Give the extent of all Plasmodium falciparum-infected red blood cells.
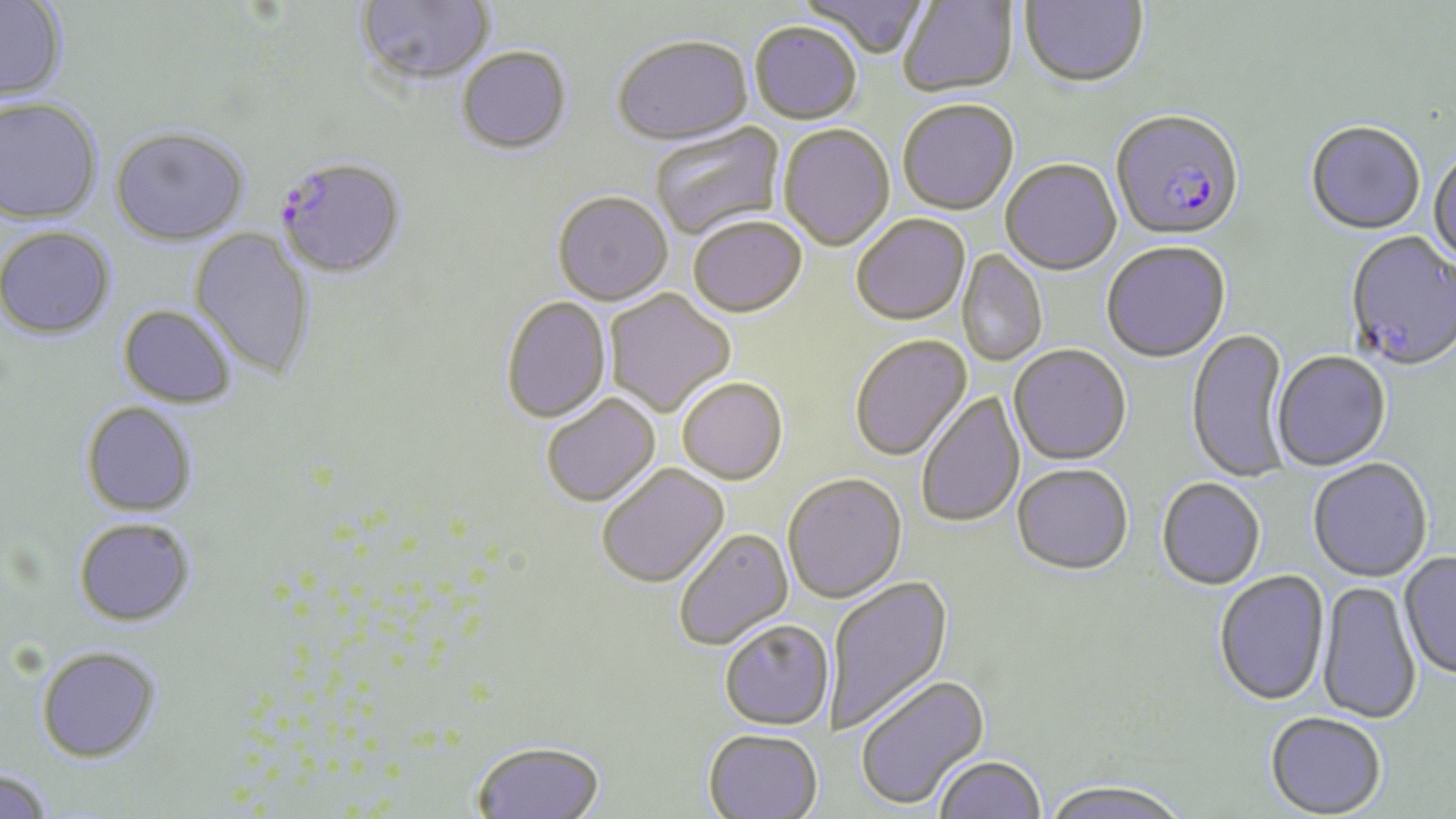
Approximate bounding boxes as [x1, y1, x2, y2] in pixels.
Plasmodium falciparum-infected red blood cells: [1110, 113, 1244, 244], [276, 157, 407, 279].

Summary:
  - Uninfected red blood cell locations: [355, 0, 494, 86], [797, 0, 930, 61], [898, 0, 1018, 98], [1020, 0, 1149, 89], [0, 1, 68, 101], [749, 24, 862, 125], [612, 37, 752, 148], [456, 47, 572, 155], [0, 96, 103, 224], [898, 101, 1019, 217], [651, 122, 786, 242], [1305, 124, 1425, 237], [110, 126, 249, 245], [778, 126, 895, 253], [1428, 151, 1456, 270], [1000, 161, 1121, 276], [552, 193, 673, 307], [851, 216, 970, 327], [688, 218, 807, 319], [0, 226, 116, 340], [188, 229, 316, 380], [1345, 233, 1455, 374], [1102, 244, 1230, 364], [957, 248, 1047, 367], [605, 290, 736, 418], [500, 296, 611, 425], [118, 305, 237, 408], [1187, 329, 1291, 484], [850, 335, 973, 463], [1008, 345, 1131, 466], [1271, 353, 1391, 472], [677, 379, 788, 486], [916, 390, 1026, 529], [541, 394, 661, 508], [81, 401, 198, 518], [1308, 459, 1432, 584], [596, 463, 730, 590], [1012, 465, 1133, 578], [782, 474, 907, 605], [1157, 479, 1265, 591], [73, 517, 196, 627], [673, 528, 794, 651], [1399, 553, 1456, 681], [1214, 571, 1330, 708], [826, 575, 955, 735], [1317, 580, 1422, 725], [719, 622, 834, 732], [36, 645, 162, 763], [855, 674, 991, 812], [1265, 713, 1386, 818], [703, 731, 823, 819], [471, 741, 606, 819], [934, 757, 1045, 818], [0, 769, 54, 819], [1040, 782, 1193, 819]
  - Slide-level diagnosis: Plasmodium falciparum
  - Field of view: single
  - Stain: May-Grünwald-Giemsa
  - Preparation: thin blood smear
  - Magnification: 1000x
  - Modality: light microscopy
  - Image size: 1456×819 pixels